Report the malaria status of this cell.
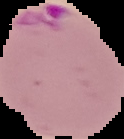
It is parasitized.

Summary:
  - Image size: 124×139 pixels
  - Preparation: thin blood film
  - Image type: segmented cell region on a black background